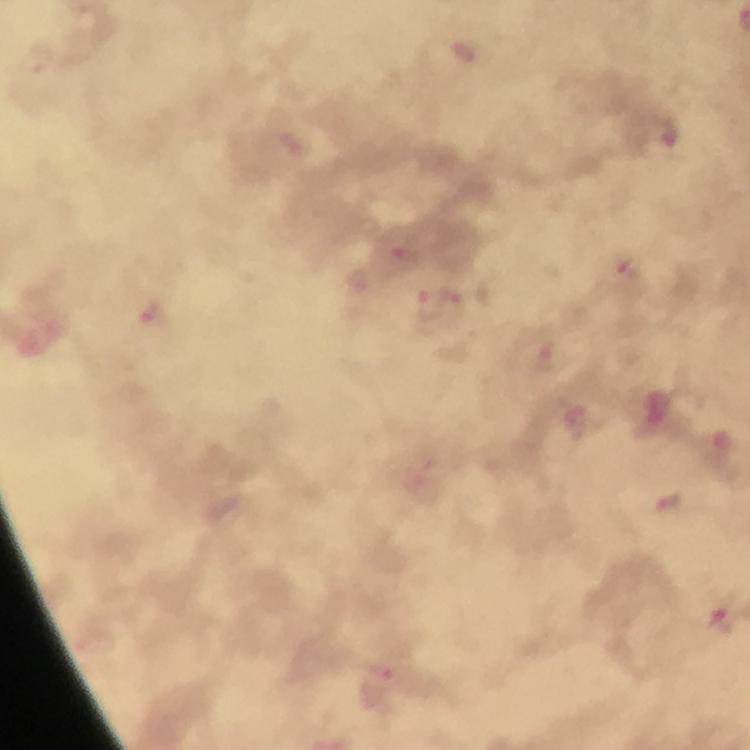
Approximate centers as [x, y] in pixels. Malaria parasite locations: [463, 55], [666, 139], [405, 254], [625, 267], [359, 278], [468, 299], [429, 303], [152, 316], [544, 357], [669, 503], [723, 619], [380, 685]. At 100x magnification. Photographed through the microscope with a smartphone camera. Cropped region of a single field of view. From a diagnostic examination for malaria. Image is 750×750 pixels. Giemsa stain. Immersion oil applied. Thick blood smear.